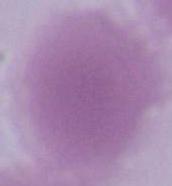

Summary:
  - Magnification: 1000x
  - Identification: red blood cell
  - Modality: photomicrograph